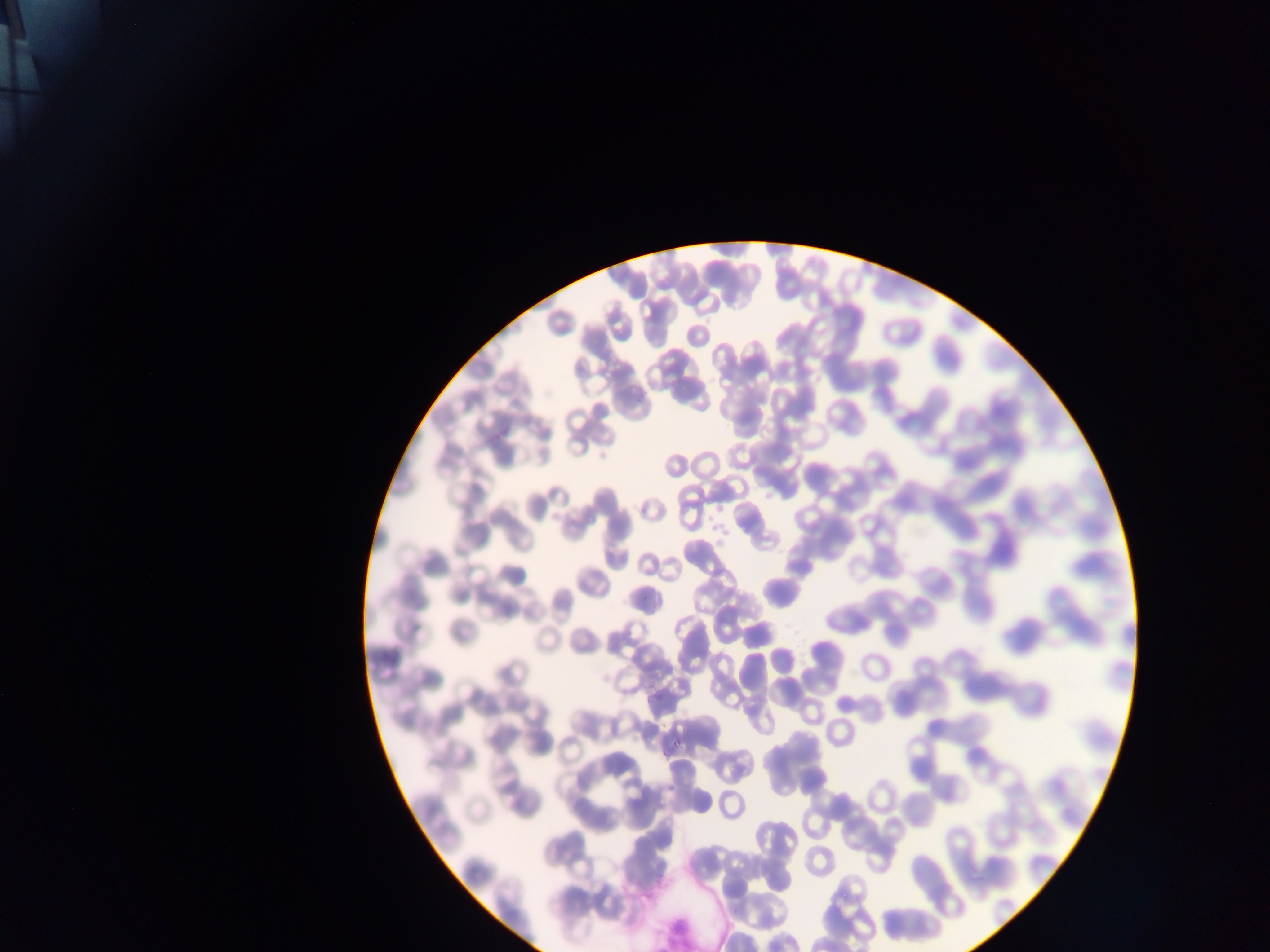

field of view = single
Plasmodium parasite locations = approximate bounding boxes as (left, top, right, bottom) in pixels: (670, 736, 685, 749)
capture = mobile-phone photograph through a microscope
image size = 1270×952 pixels
preparation = thin blood smear
artifact (stain precipitate or debris) locations = approximate bounding boxes as (left, top, right, bottom) in pixels: (648, 902, 701, 950)
country = Ghana